Identify the parasite.
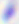

Toxoplasma gondii.

{
  "magnification": "400x",
  "modality": "micrograph"
}